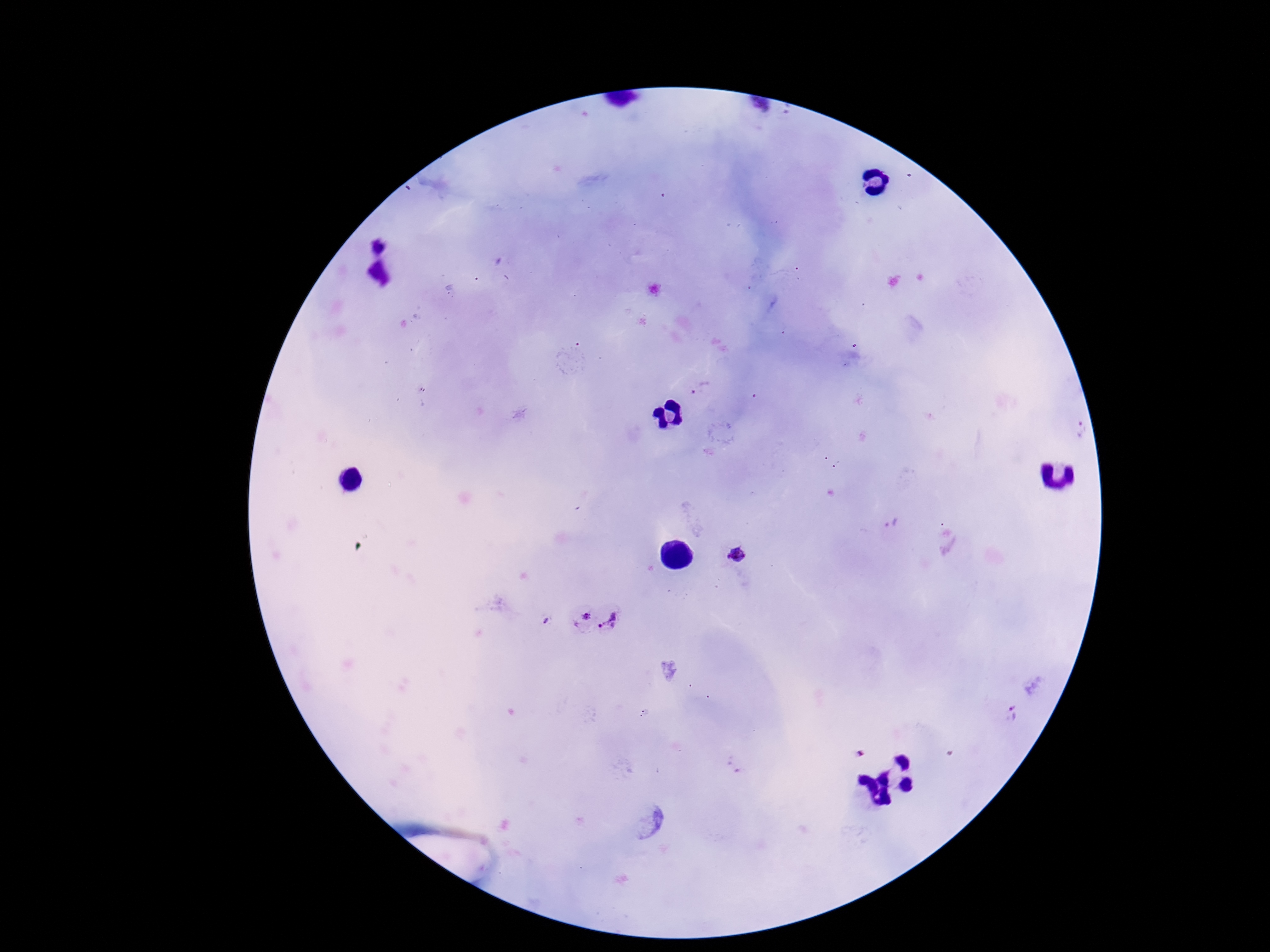
Approximate centers as {x, y} in pixels.
Summary:
  - Plasmodium parasite locations: {702, 388}, {1079, 430}, {737, 555}, {579, 618}, {612, 619}, {546, 620}, {1011, 715}, {859, 752}
  - Image size: 1270×952 pixels
  - Patient malaria status: positive
  - Stain: Giemsa
  - Magnification: 100x
  - Preparation: thick blood smear
  - Field of view: one from this slide
  - Capture: smartphone camera through the microscope eyepiece